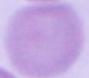

1000x magnification. Micrograph. A red blood cell is seen.